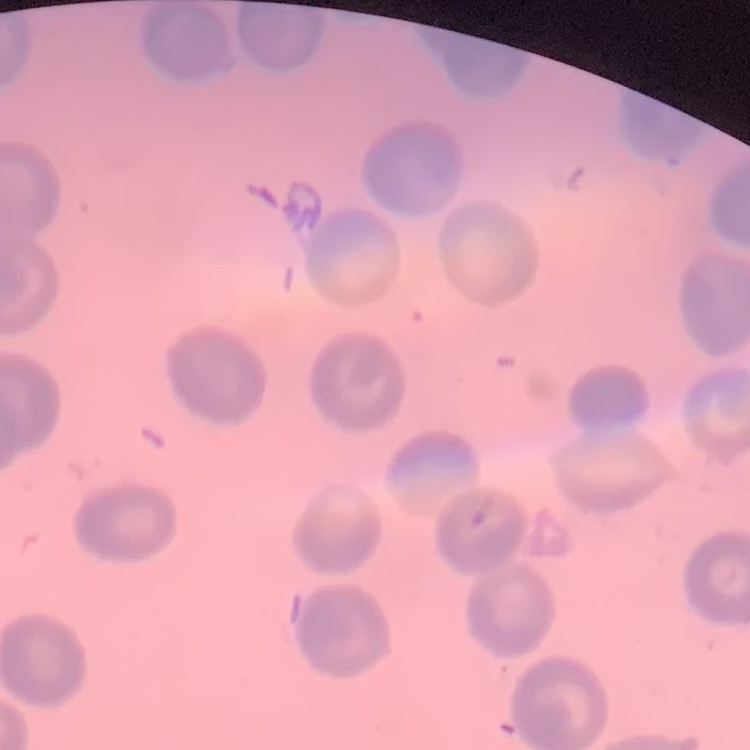

Summary:
  - Erythrocyte morphology: no rouleaux formation
  - Preparation: thin blood smear
  - Image type: one tile cut from a larger photomicrograph
  - Stain: Field's or Giemsa